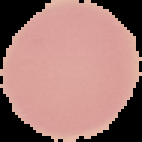
Summary:
  - Preparation: thin blood smear
  - Image type: segmented cell region with the area outside set to black
  - Image size: 142×142 pixels
  - Result: negative for malaria parasites